Assess this cell for malaria.
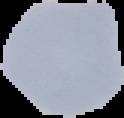

It is uninfected.

{
  "image_size": "124×118 pixels",
  "image_type": "segmented cell region with the area outside set to black",
  "preparation": "thin blood smear"
}